Comment on the morphology of the red blood cells.
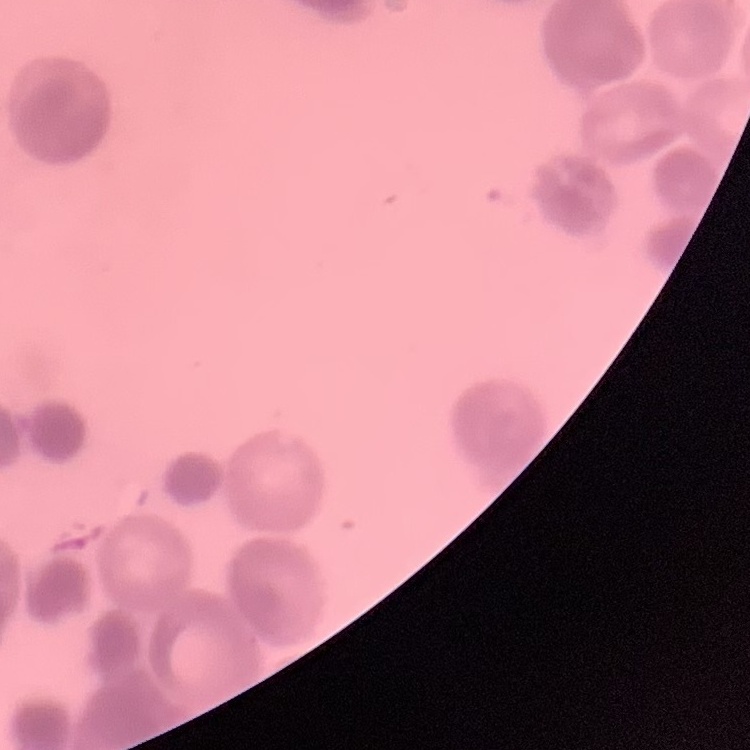

They show rouleaux formation.

One tile cut from a larger photomicrograph. Thin blood smear. Field's or Giemsa stain.